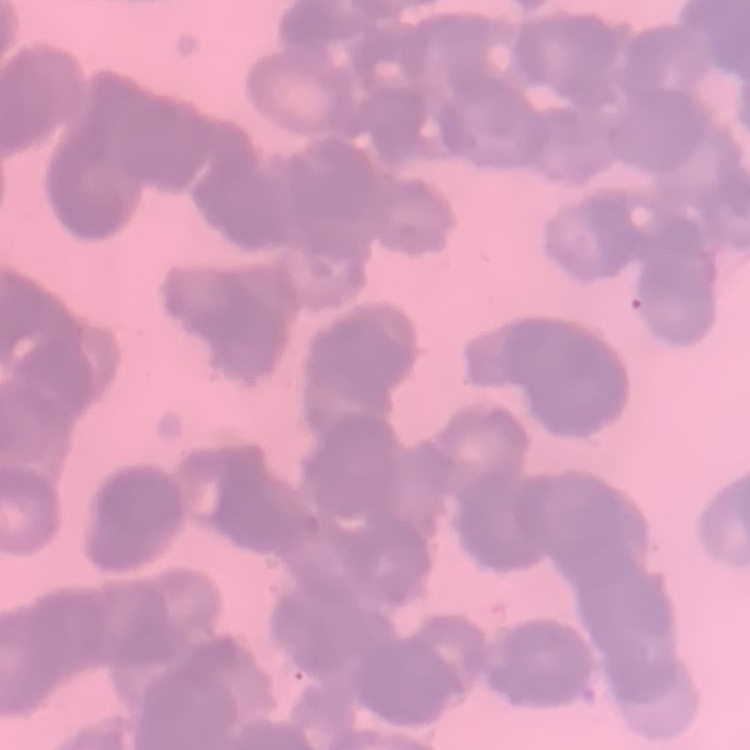
The erythrocytes exhibit rouleaux formation. Thin peripheral smear. One tile cut from a larger photomicrograph. Field's or Giemsa stain.